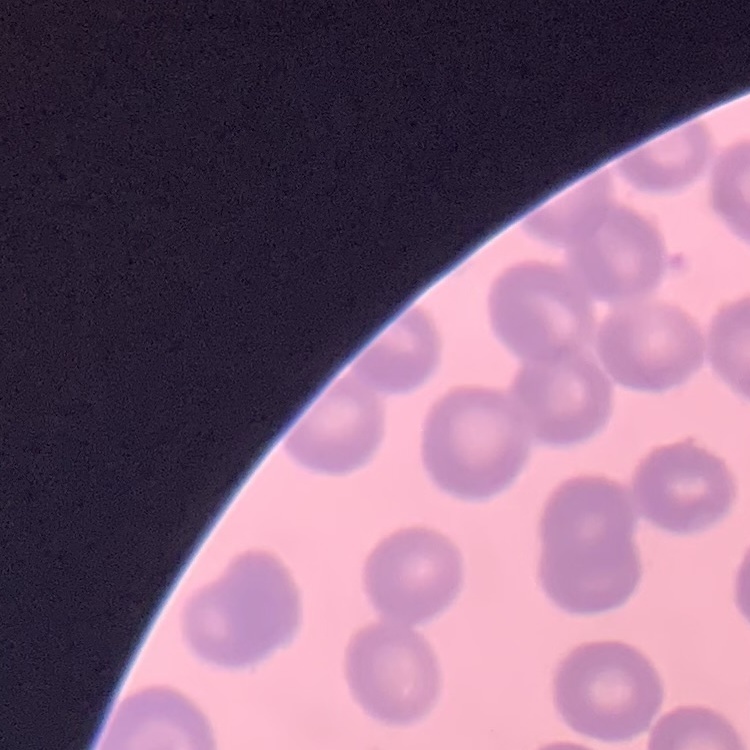

Summary:
  - Red blood cell morphology: no rouleaux formation
  - Stain: Field's or Giemsa
  - Preparation: thin blood film
  - Image type: one tile cut from a larger photomicrograph